Assess this cell for malaria.
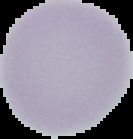

It is uninfected.

From a thin blood smear. Image is 133×139 pixels. The area outside the segmented cell region is set to black.